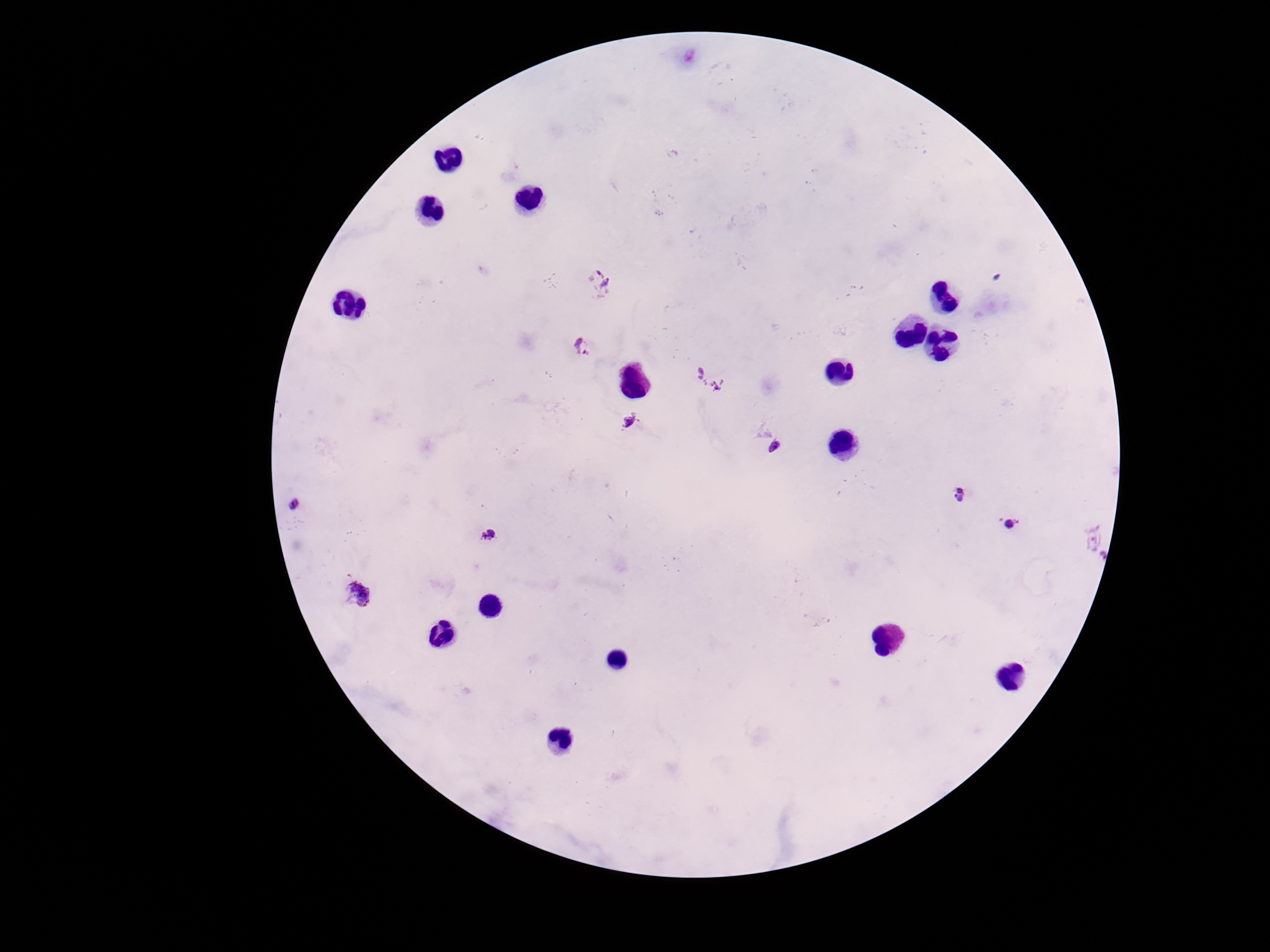
patient_malaria_status: positive
magnification: 100x
image_size: 1270×952 pixels
preparation: thick peripheral-blood smear
capture: smartphone camera through the microscope eyepiece
field_of_view: one from this slide
plasmodium_parasite_locations: 'approximate object centers, in pixels from the top-left corner: (x=596, y=283), (x=582, y=348), (x=710, y=378), (x=630, y=421), (x=775, y=446), (x=960, y=495), (x=295, y=504), (x=1008, y=524), (x=488, y=535), (x=1102, y=544), (x=360, y=594)'
stain: Giemsa